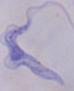
Summary:
  - Modality: photomicrograph
  - Magnification: 1000x
  - Identification: trypanosome